Identify the cell.
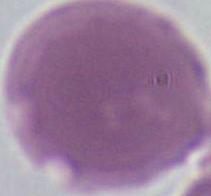
An erythrocyte.

{
  "modality": "photomicrograph",
  "magnification": "1000x"
}